Point out each Plasmodium parasite.
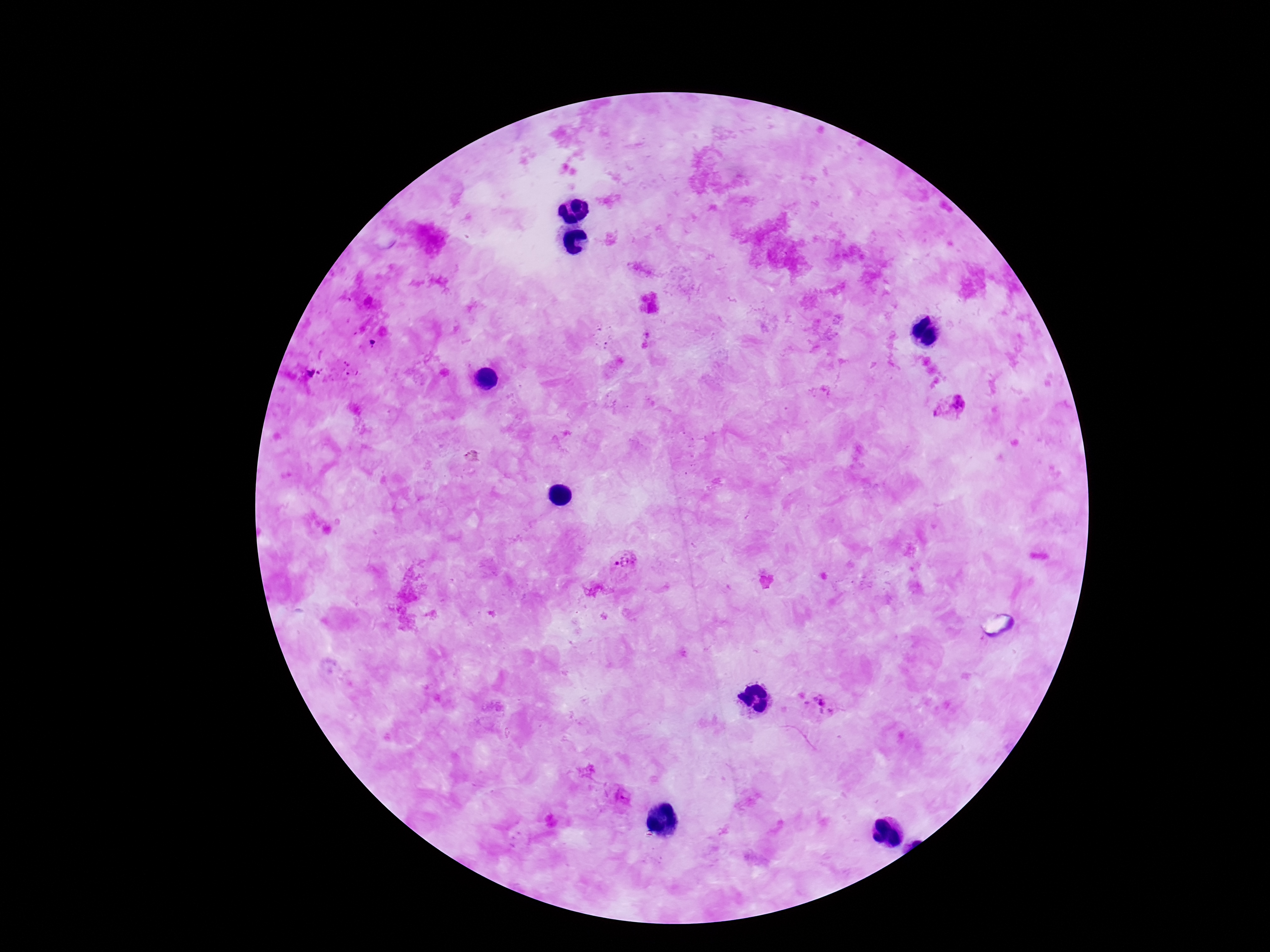

Approximate object centers, in pixels from the top-left corner.
Plasmodium parasites: (x=959, y=404), (x=938, y=410), (x=625, y=560), (x=820, y=706), (x=621, y=796).

Giemsa-stained preparation. Thick peripheral-blood smear. Smartphone photograph taken through the microscope eyepiece. One field from this slide. Patient malaria status: positive. Image is 1270×952 pixels. 100x magnification.